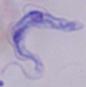
Summary:
  - Magnification: 1000x
  - Identification: trypanosome
  - Modality: photomicrograph